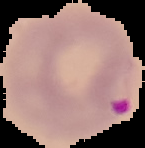
Summary:
  - Malaria status: parasitized
  - Image size: 145×148 pixels
  - Image type: segmented cell region with the area outside set to black
  - Preparation: thin blood smear